Report the malaria status of this cell.
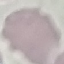
Uninfected.

Summary:
  - Image type: automatically extracted cell patch, resized to 64 × 64 pixels
  - Preparation: thin blood film
  - Capture: smartphone camera at the microscope eyepiece
  - Stain: Giemsa